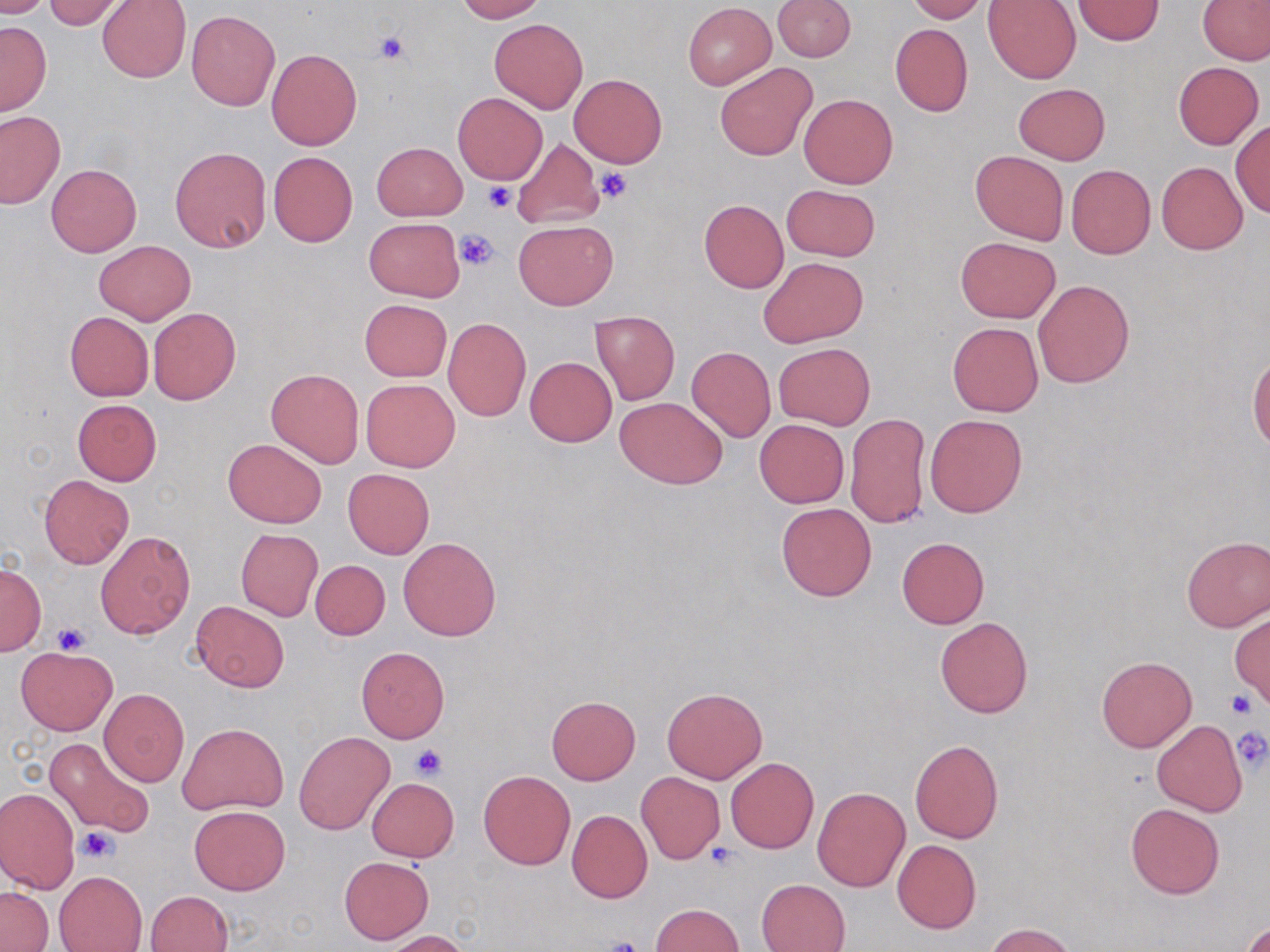

Summary:
  - Coordinate format: approximate bounding boxes as (x1, y1, x2, y2) in pixels
  - Uninfected red blood cell locations: (0, 0, 54, 18), (42, 0, 130, 30), (453, 0, 547, 21), (772, 0, 854, 61), (905, 0, 986, 22), (1072, 0, 1165, 45), (97, 1, 191, 83), (983, 1, 1080, 83), (1199, 1, 1269, 65), (683, 3, 775, 88), (187, 10, 279, 110), (489, 18, 588, 114), (0, 21, 51, 115), (890, 23, 973, 116), (266, 48, 363, 150), (715, 62, 816, 161), (1174, 62, 1264, 148), (570, 74, 667, 168), (1013, 83, 1110, 164), (452, 91, 548, 185), (799, 93, 898, 189), (0, 111, 65, 208), (1230, 120, 1270, 217), (512, 136, 604, 230), (371, 142, 466, 221), (169, 146, 270, 253), (268, 150, 359, 248), (970, 150, 1068, 244), (1157, 162, 1247, 254), (46, 164, 140, 256), (1067, 165, 1155, 259), (781, 184, 880, 260), (698, 200, 788, 293), (364, 218, 464, 300), (513, 219, 618, 309), (955, 236, 1061, 322), (93, 240, 194, 324), (759, 256, 868, 348), (1033, 279, 1134, 388), (360, 299, 451, 381), (148, 307, 241, 405), (590, 310, 679, 405), (64, 311, 153, 401), (443, 318, 531, 421), (948, 322, 1043, 416), (774, 342, 874, 430), (687, 346, 776, 441), (1247, 355, 1270, 453), (525, 357, 615, 447), (266, 368, 364, 467), (361, 378, 460, 471), (615, 396, 727, 488), (72, 399, 162, 485), (845, 413, 930, 529), (925, 414, 1026, 517), (754, 419, 849, 507), (223, 438, 327, 527), (343, 468, 434, 558), (38, 474, 134, 569), (777, 502, 876, 601), (236, 528, 322, 621), (94, 531, 194, 639), (1181, 535, 1270, 631), (398, 536, 501, 641), (896, 537, 988, 629), (311, 560, 389, 640), (0, 564, 45, 655), (191, 601, 287, 691), (1230, 612, 1269, 708), (936, 616, 1033, 717), (16, 646, 117, 735), (356, 646, 449, 742), (1096, 655, 1197, 752), (663, 687, 766, 783), (99, 689, 189, 786), (546, 695, 640, 785), (62, 701, 171, 815), (1151, 720, 1247, 817), (178, 722, 287, 814), (294, 732, 394, 835), (44, 736, 155, 839), (910, 738, 1004, 844), (726, 758, 819, 853), (479, 771, 575, 869), (635, 773, 724, 863), (366, 778, 460, 862), (0, 787, 81, 893), (813, 787, 910, 891), (1126, 804, 1225, 899), (189, 806, 290, 895), (567, 810, 652, 903), (892, 839, 981, 933), (339, 856, 433, 944), (55, 871, 147, 952), (757, 879, 850, 952), (0, 886, 52, 951), (145, 890, 234, 952), (650, 903, 744, 952), (1240, 917, 1269, 952), (984, 923, 1076, 952), (386, 930, 472, 952)
  - Platelet locations: (375, 33, 410, 64), (596, 168, 633, 203), (483, 183, 516, 213), (455, 228, 499, 270), (51, 621, 90, 655), (1226, 690, 1257, 717), (1231, 727, 1269, 771), (410, 743, 448, 779), (77, 825, 119, 863), (703, 843, 739, 870), (598, 936, 644, 952)
  - Slide-level diagnosis: no evidence of blood parasites
  - Image size: 1270×952 pixels
  - Magnification: 1000x
  - Preparation: thin blood film
  - Modality: light microscopy
  - Field of view: one of a larger specimen
  - Stain: May-Grünwald-Giemsa